Locate every malaria parasite.
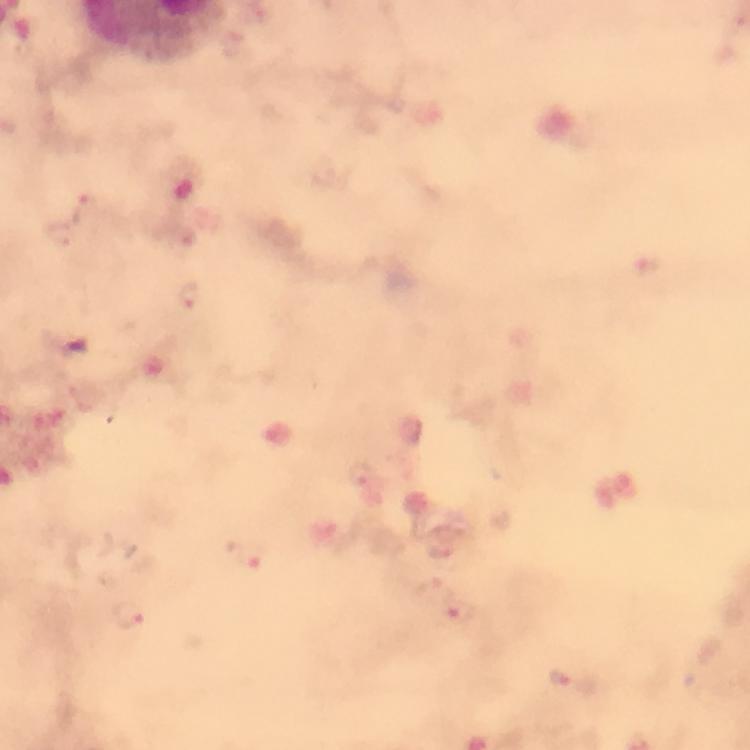

Approximate centers as (x, y) in pixels.
Malaria parasites: (88, 204), (129, 612), (463, 612), (565, 677).

Summary:
  - Capture: smartphone mounted on the microscope
  - Stain: Giemsa
  - Immersion oil: applied
  - Magnification: 100x
  - Preparation: thick blood film
  - Cropped from: one field of view
  - Context: from a malaria diagnostic workup
  - Image size: 750×750 pixels